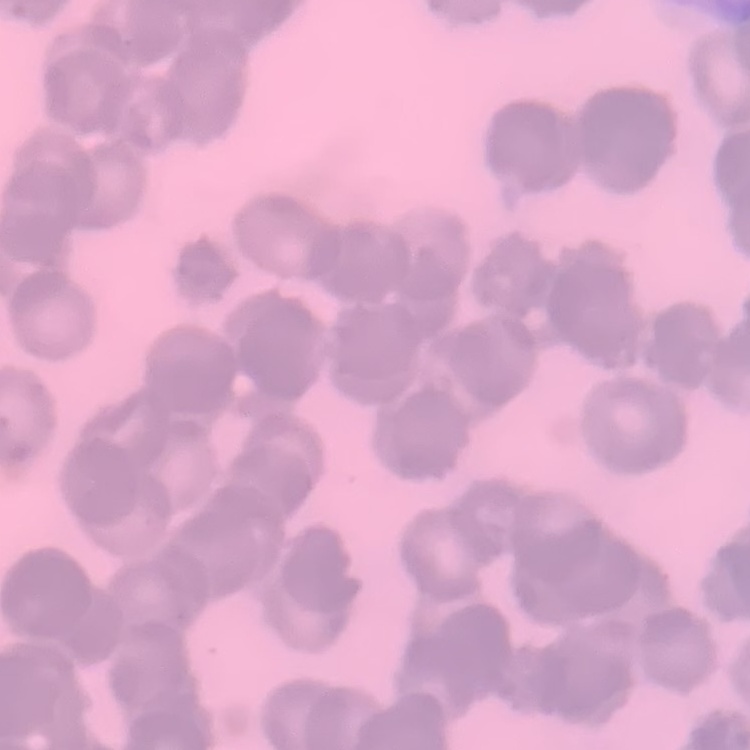

The erythrocytes exhibit rouleaux formation. Field's or Giemsa stain. Square crop of a larger photomicrograph. Thin peripheral smear.